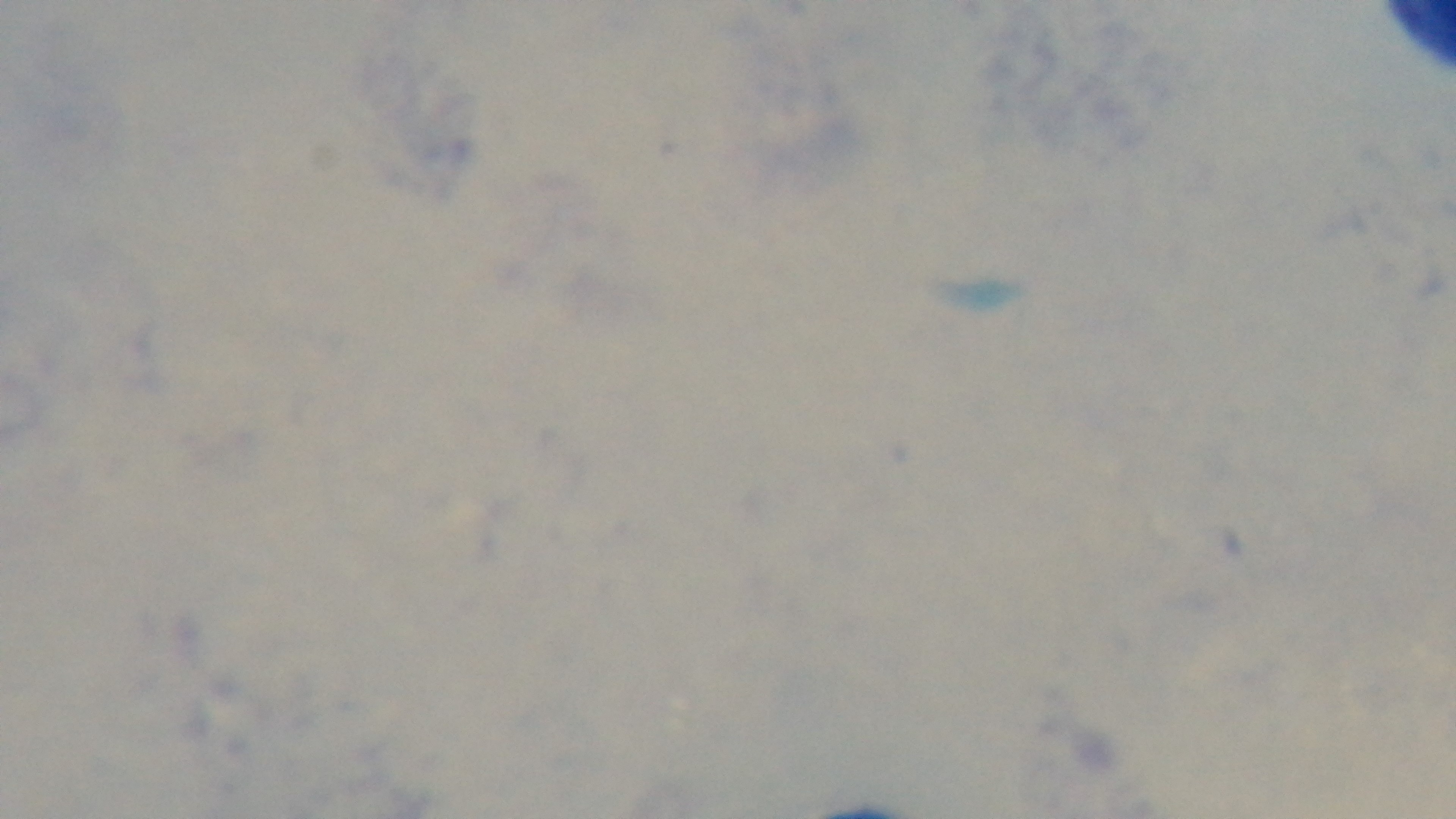
Summary:
  - Modality: light microscopy
  - Capture: mounted 4K digital camera
  - Malaria status: negative
  - Stain: Giemsa
  - Field of view: one from the slide
  - Preparation: thick smear
  - Objective: 100x oil immersion